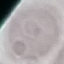
Summary:
  - Malaria status: uninfected
  - Capture: smartphone through the microscope eyepiece
  - Preparation: thin smear
  - Stain: Giemsa
  - Image type: automatically extracted cell patch, resized to 64 × 64 pixels